Give the extent of all uninfected red blood cells.
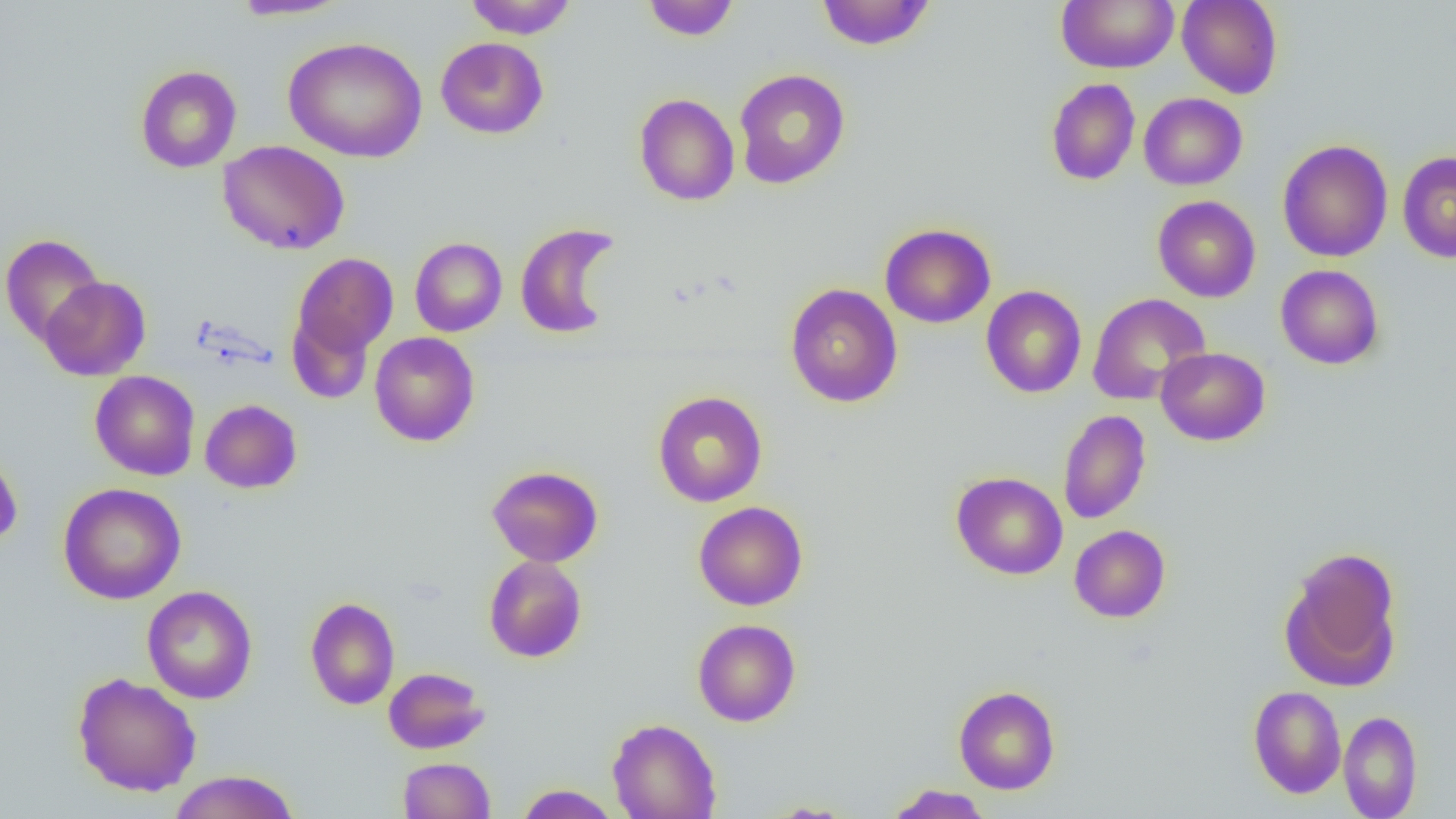
Approximate bounding boxes as (x1, y1, x2, y2) in pixels.
Uninfected red blood cells: (231, 0, 351, 20), (465, 0, 577, 39), (642, 0, 740, 41), (815, 0, 936, 51), (1056, 0, 1179, 74), (1176, 0, 1283, 99), (283, 36, 428, 163), (435, 37, 548, 139), (135, 65, 242, 173), (734, 68, 850, 189), (1046, 78, 1140, 185), (1138, 92, 1247, 190), (634, 93, 739, 206), (1278, 139, 1393, 263), (218, 140, 350, 255), (1397, 151, 1456, 263), (1152, 195, 1261, 302), (514, 222, 621, 341), (880, 223, 996, 328), (0, 234, 106, 348), (409, 237, 507, 337), (291, 253, 398, 360), (1275, 265, 1384, 370), (39, 276, 151, 381), (785, 283, 903, 408), (981, 285, 1086, 398), (1087, 293, 1211, 405), (286, 309, 376, 404), (369, 332, 480, 447), (1155, 347, 1270, 446), (90, 370, 200, 481), (652, 390, 768, 507), (200, 399, 302, 493), (1058, 409, 1151, 525), (0, 448, 23, 551), (487, 465, 603, 567), (951, 471, 1067, 579), (58, 482, 186, 605), (693, 501, 808, 611), (1069, 525, 1170, 623), (1281, 546, 1403, 691), (484, 555, 587, 663), (141, 586, 257, 704), (304, 596, 400, 710), (692, 618, 801, 727), (383, 666, 490, 754), (72, 672, 201, 796), (1248, 685, 1346, 799), (954, 686, 1060, 794), (1338, 710, 1423, 819), (607, 717, 722, 819), (398, 757, 495, 818), (168, 770, 301, 819), (516, 784, 621, 819), (884, 784, 993, 819), (759, 801, 860, 817).

slide-level diagnosis = no evidence of blood parasites
field of view = one of a larger specimen
preparation = thin blood smear
image size = 1456×819 pixels
modality = light microscopy
magnification = 1000x